Identify the parasite.
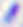

This is Toxoplasma gondii.

Micrograph. 400x magnification.